Describe the morphology of the erythrocytes.
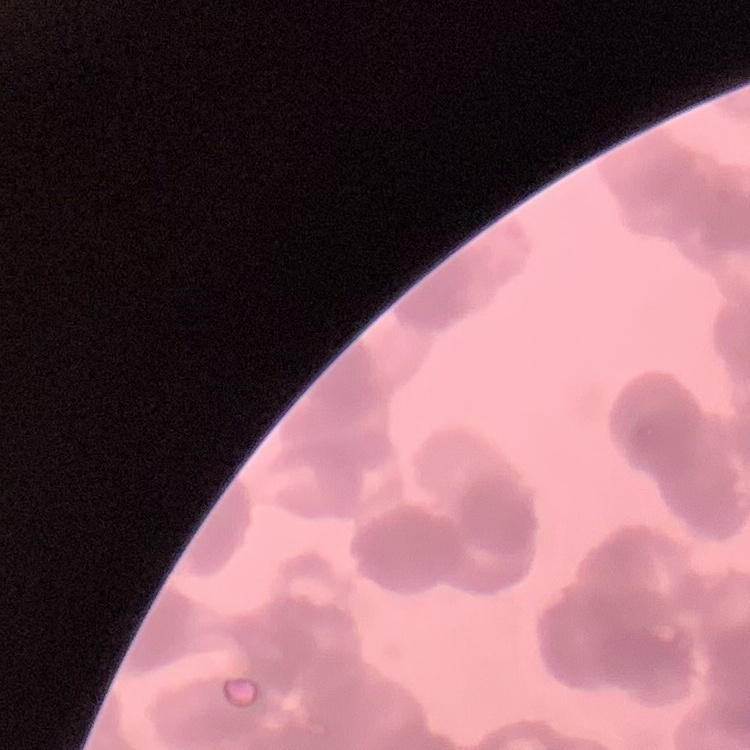
Rouleaux formation.

Thin blood smear. Square crop of a larger photomicrograph. Stained with either Field's or Giemsa.